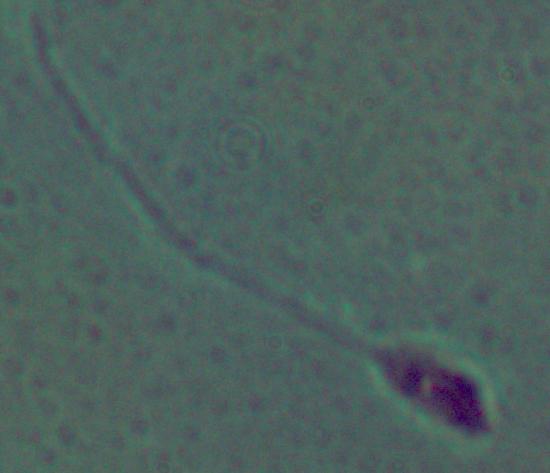
{
  "identification": "Leishmania",
  "modality": "micrograph",
  "magnification": "1000x"
}